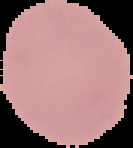

Summary:
  - Result: no Plasmodium parasites detected
  - Image type: cell region segmented out of the field of view; surrounding area masked to black
  - Image size: 133×148 pixels
  - Preparation: thin blood film